Assess this cell for malaria.
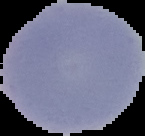
It is uninfected.

image size = 145×136 pixels
image type = segmented cell region on a black background
preparation = thin blood film